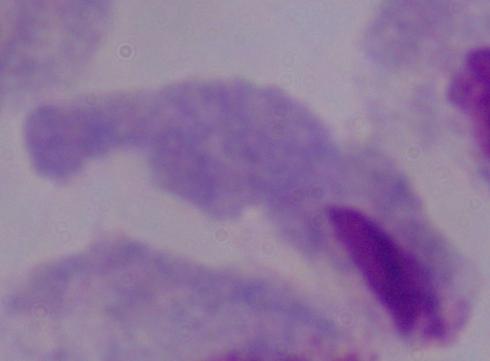
Summary:
  - Identification: trichomonad
  - Magnification: 1000x
  - Modality: photomicrograph